Report the malaria status of this cell.
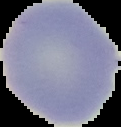
It is uninfected.

Summary:
  - Preparation: thin blood film
  - Image type: segmented cell region with the area outside set to black
  - Image size: 121×127 pixels